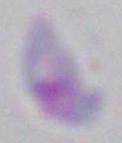

{
  "modality": "micrograph",
  "magnification": "1000x",
  "identification": "Toxoplasma gondii"
}